Classify this cell by malaria status.
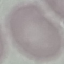

It is uninfected.

image_type: cell patch, automatically extracted from a larger field of view and resized to 64 × 64 pixels
stain: Giemsa
capture: smartphone through the microscope eyepiece
preparation: thin smear